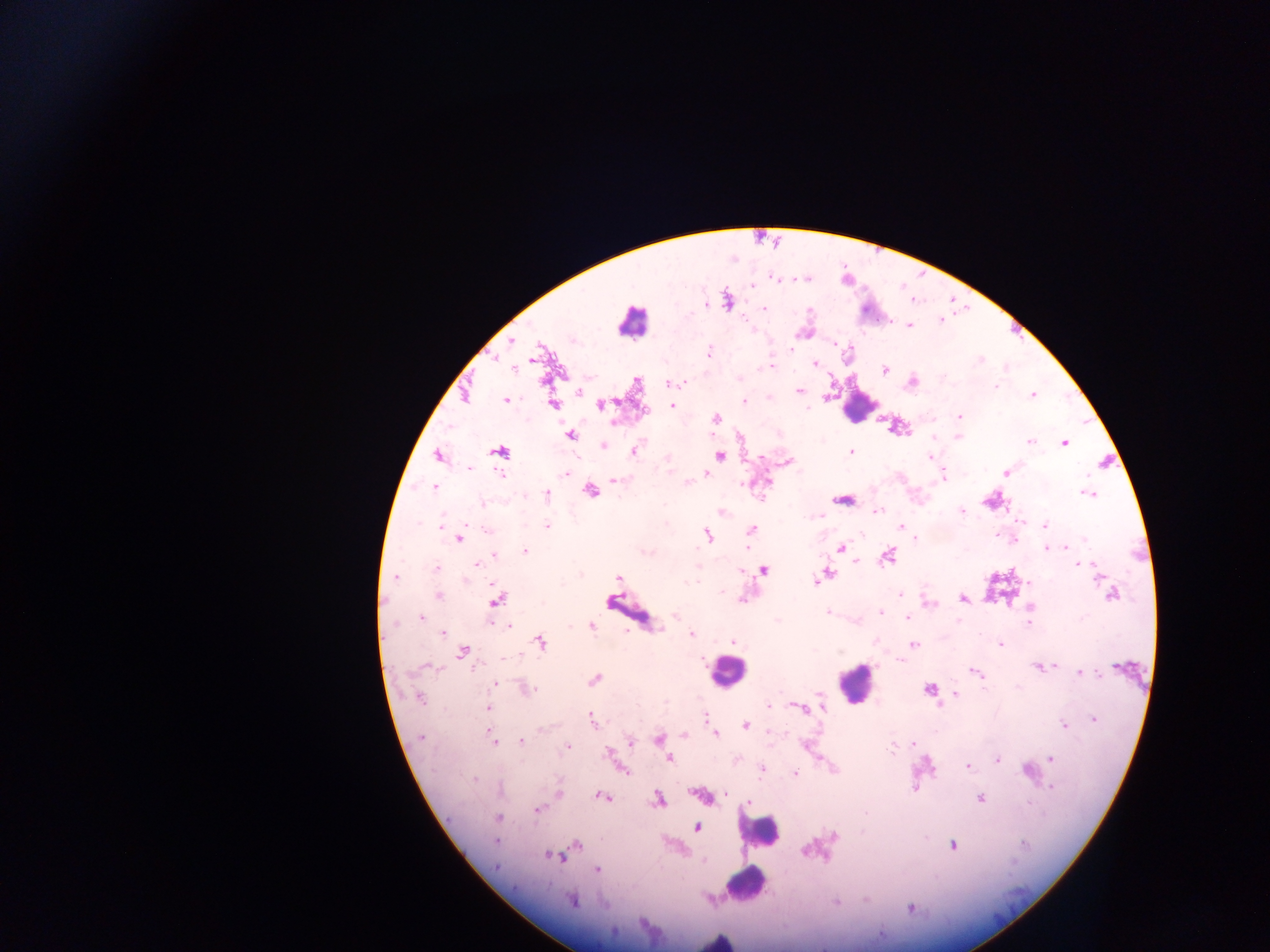
Approximate centers as x y in pixels. Leukocyte locations: 630 321; 859 406; 630 612; 726 670; 855 683; 759 832; 744 883; 717 940. Plasmodium parasite locations: 773 277; 751 285; 727 300; 764 308; 940 322; 909 325; 805 332; 511 341; 834 344; 708 353; 534 356; 814 363; 773 366; 884 370; 911 382; 671 383; 578 391; 798 391; 464 394; 1032 394; 506 399; 743 400; 553 403; 600 404; 671 406; 958 416; 716 418; 614 421; 897 427; 569 434; 958 436; 1029 440; 1064 442; 603 446; 634 449; 500 451; 851 452; 437 455; 720 455; 930 455; 788 461; 1005 471; 566 474; 706 474; 942 474; 615 480; 688 481; 765 482; 433 487; 589 491; 546 493; 1089 493; 841 499; 991 500; 722 511; 876 511; 962 511; 1045 525; 441 526; 546 526; 899 527; 750 530; 707 535; 458 538; 840 549; 1046 549; 524 550; 494 555; 887 556; 1078 564; 436 569; 763 570; 822 575; 395 577; 618 578; 900 593; 1111 594; 439 595; 742 598; 962 598; 496 599; 1030 607; 829 612; 880 612; 908 615; 420 616; 1028 622; 507 625; 591 625; 442 633; 691 634; 734 641; 539 642; 1000 644; 913 645; 463 651; 1039 666; 975 672; 1079 673; 594 680; 493 683; 524 688; 929 688; 955 693; 418 697; 820 697; 821 705; 802 707; 487 709; 704 716; 1093 718; 592 720; 745 724; 1064 724; 683 734; 715 734; 421 738; 658 739; 492 740; 630 740; 520 741; 912 744; 567 746; 663 749; 608 753; 1051 758; 668 759; 997 760; 968 766; 762 768; 623 769; 1028 772; 794 773; 915 788; 1051 788; 558 794; 701 795; 602 796; 980 797; 658 799; 748 802; 537 809; 498 817; 697 826; 494 840; 575 844; 952 845; 561 853; 552 855; 560 856; 495 866; 597 870; 573 900; 836 902; 910 908. Sample from Ghana. Thick blood film. Image is 1270×952 pixels. Mobile-phone photograph taken through the microscope. Single field of view.